Locate every Plasmodium vivax-infected red blood cell.
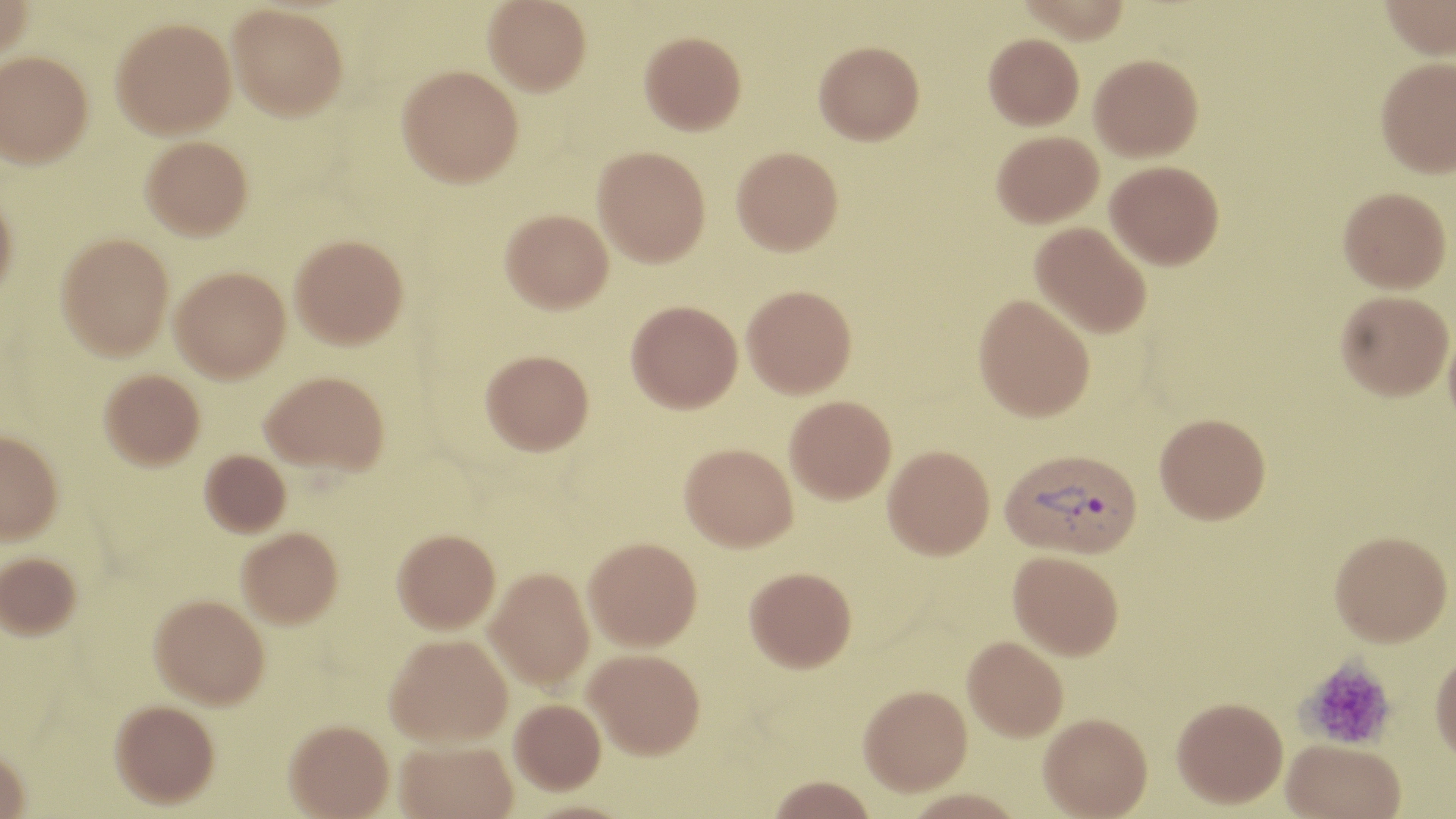

Approximate bounding boxes as (x1, y1, x2, y2) in pixels.
Plasmodium vivax-infected red blood cells: (999, 449, 1143, 561).

Platelet locations: (1297, 655, 1397, 752). Uninfected red blood cell locations: (0, 0, 33, 61), (484, 0, 592, 95), (1378, 0, 1456, 61), (227, 3, 349, 120), (111, 17, 236, 137), (639, 31, 746, 134), (983, 33, 1084, 129), (814, 40, 924, 144), (0, 50, 94, 168), (1089, 53, 1203, 160), (1375, 56, 1456, 178), (397, 65, 523, 186), (992, 130, 1103, 227), (140, 135, 253, 240), (593, 146, 710, 266), (732, 146, 843, 255), (1105, 160, 1224, 269), (1338, 186, 1451, 292), (0, 193, 17, 303), (500, 208, 613, 313), (1030, 221, 1152, 339), (56, 233, 174, 359), (290, 234, 408, 348), (170, 266, 290, 382), (742, 284, 856, 397), (1336, 290, 1453, 399), (974, 293, 1095, 422), (626, 300, 742, 413), (1444, 319, 1456, 437), (481, 349, 594, 454), (99, 369, 205, 470), (260, 369, 389, 474), (785, 395, 897, 505), (1154, 414, 1270, 525), (0, 429, 63, 545), (679, 444, 798, 553), (883, 445, 995, 563), (200, 450, 291, 537), (236, 527, 343, 628), (392, 529, 500, 635), (1329, 532, 1452, 650), (583, 538, 702, 653), (0, 551, 82, 639), (1007, 552, 1123, 662), (486, 568, 595, 692), (744, 570, 856, 676), (149, 594, 268, 708), (385, 636, 512, 748), (962, 638, 1068, 745), (584, 651, 704, 763), (1430, 651, 1456, 768), (859, 688, 973, 801), (110, 699, 219, 807), (509, 700, 606, 797), (1172, 700, 1288, 813), (1039, 717, 1153, 819), (284, 721, 394, 819), (395, 741, 518, 819), (1281, 743, 1405, 819), (0, 747, 31, 818), (766, 779, 878, 818), (902, 793, 1029, 819). Slide-level diagnosis: Plasmodium vivax. Captured at 1000x magnification. Thin blood film. Image is 1456×819 pixels. Single field of view. Light microscopy. May-Grünwald-Giemsa-stained preparation.